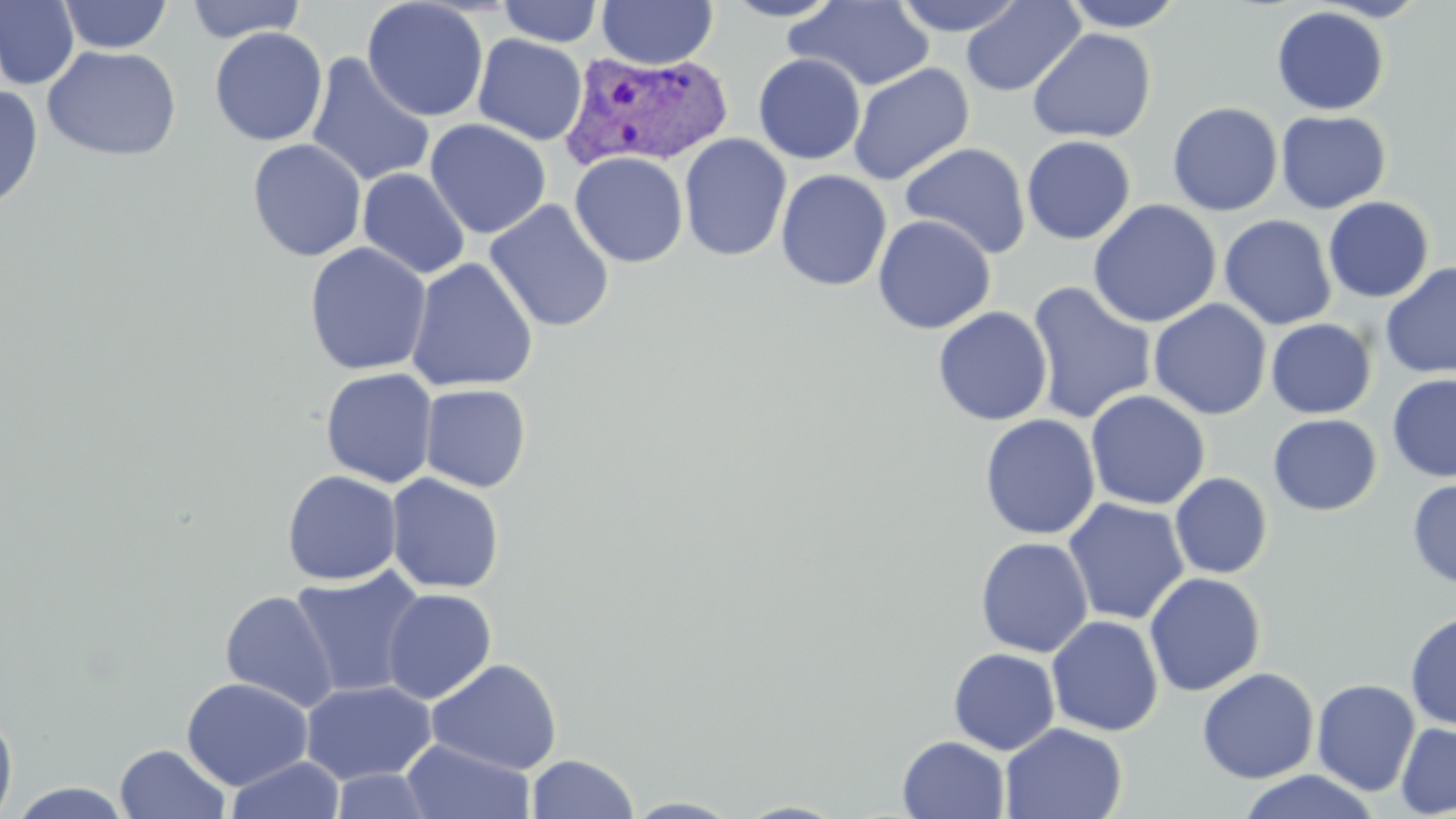
Approximate bounding boxes as (x1,y1)-(x2,y2) corner pairs in pixels. Uninfected red blood cell locations: (0,0)-(80,90), (57,0)-(174,54), (184,0)-(306,43), (361,0)-(489,122), (596,0)-(718,69), (720,0)-(846,22), (890,0)-(1028,36), (960,0)-(1086,97), (1057,0)-(1190,32), (496,1)-(605,47), (785,1)-(935,92), (1271,6)-(1390,116), (209,26)-(329,146), (1028,28)-(1156,143), (472,34)-(588,145), (42,45)-(181,161), (305,53)-(436,187), (752,53)-(866,164), (848,63)-(974,185), (0,83)-(44,213), (1167,102)-(1283,216), (1275,110)-(1391,213), (424,119)-(552,239), (678,133)-(792,261), (1021,135)-(1136,245), (247,138)-(367,262), (900,142)-(1031,259), (570,152)-(689,267), (357,167)-(470,280), (774,169)-(892,291), (1323,197)-(1434,303), (484,199)-(615,334), (1088,199)-(1222,328), (1219,214)-(1337,330), (872,215)-(996,334), (303,242)-(432,376), (405,257)-(539,393), (1380,263)-(1456,378), (1026,281)-(1157,425), (1148,299)-(1272,421), (932,307)-(1053,427), (1266,318)-(1377,419), (320,367)-(438,488), (1387,373)-(1456,482), (420,384)-(532,493), (1085,390)-(1210,510), (1267,413)-(1382,515), (979,414)-(1100,540), (282,469)-(402,585), (1169,472)-(1273,579), (386,473)-(505,595), (1407,478)-(1456,589), (1062,497)-(1189,626), (975,536)-(1093,657), (289,567)-(426,699), (1144,572)-(1266,696), (382,588)-(497,704), (220,589)-(340,711), (1405,610)-(1456,731), (1046,615)-(1164,736), (948,647)-(1060,755), (426,658)-(563,775), (1196,667)-(1319,784), (181,677)-(313,790), (1311,678)-(1421,796), (300,679)-(437,785), (0,704)-(18,819), (1395,722)-(1456,818), (1000,723)-(1127,819), (896,735)-(1009,819), (400,738)-(536,819), (114,743)-(230,818), (526,753)-(638,818), (225,756)-(344,818), (327,768)-(438,818), (1235,770)-(1381,819), (6,782)-(136,819), (623,796)-(745,818), (732,800)-(851,819). Plasmodium vivax-infected red blood cell locations: (561,50)-(734,172). Slide-level diagnosis: Plasmodium vivax. Image is 1456×819 pixels. Thin blood smear. May-Grünwald-Giemsa-stained preparation. One field of a larger specimen. Optical microscopy. 1000x magnification.